Identify the cell.
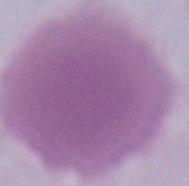

An erythrocyte.

Photomicrograph. Captured at 1000x magnification.